Classify this cell by malaria status.
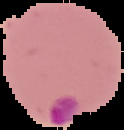
It is parasitized.

From a thin blood film. The area outside the segmented cell region is set to black. Image is 124×130 pixels.